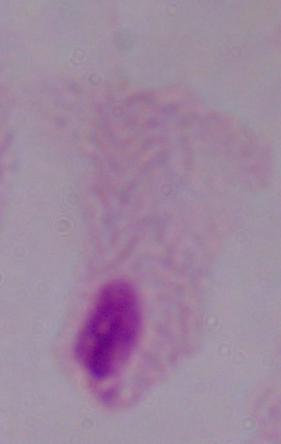

Summary:
  - Identification: trichomonad
  - Modality: photomicrograph
  - Magnification: 1000x